Assess this cell for malaria.
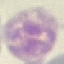
Uninfected.

Summary:
  - Preparation: thin blood smear
  - Capture: smartphone through the microscope eyepiece
  - Stain: Giemsa
  - Image type: cell patch, automatically extracted from a larger field of view and resized to 64 × 64 pixels